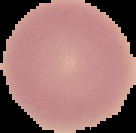
Summary:
  - Preparation: thin blood film
  - Image type: segmented cell region with the area outside set to black
  - Image size: 136×133 pixels
  - Malaria status: uninfected